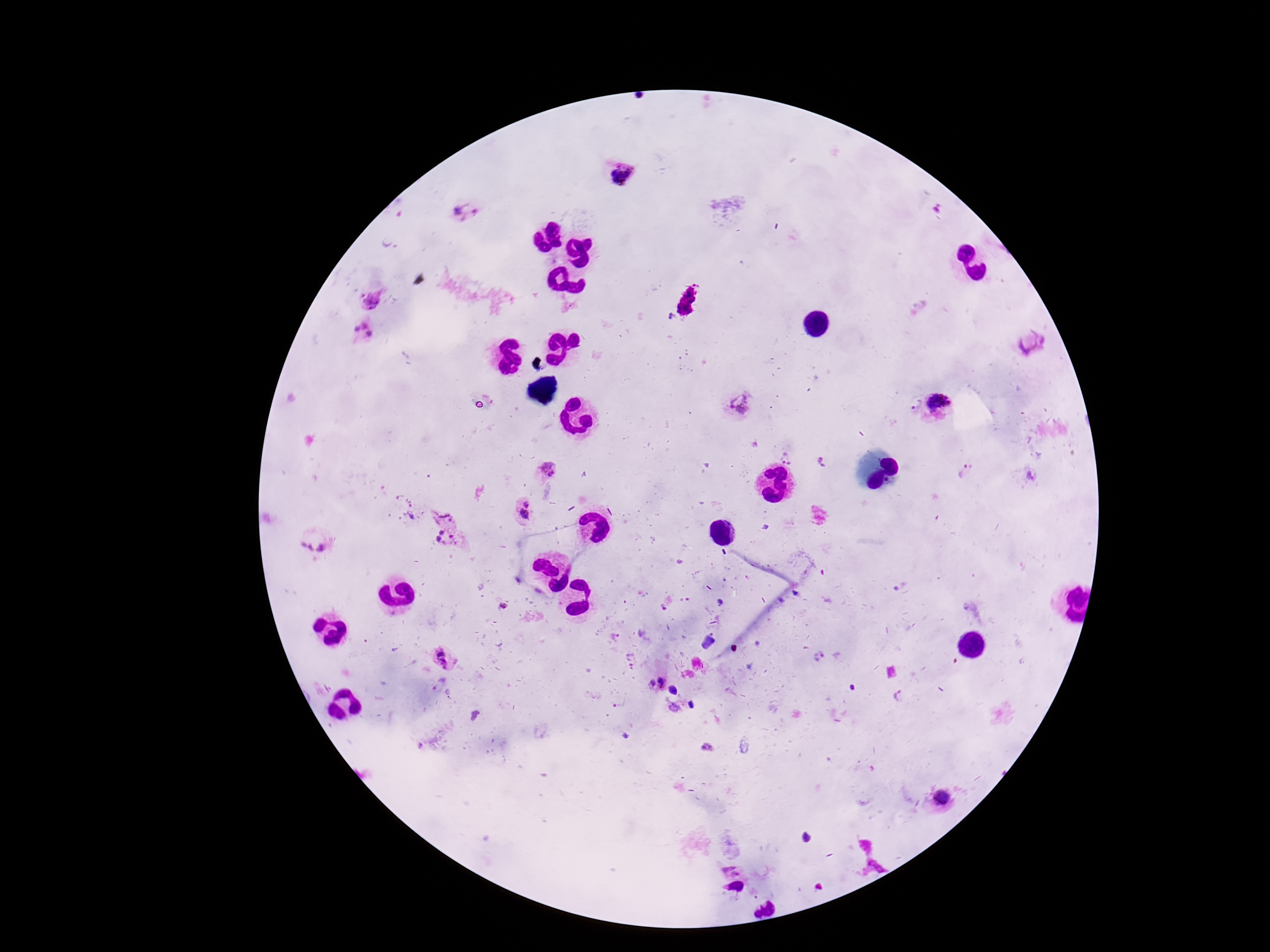
capture = smartphone camera through the microscope eyepiece
preparation = thick blood film
field of view = single
Plasmodium parasite locations = approximate centers as {x, y} in pixels: {621, 177}, {462, 212}, {373, 303}, {360, 334}, {1029, 344}, {913, 405}, {939, 407}, {738, 408}, {788, 452}, {548, 468}, {968, 471}, {409, 508}, {523, 512}, {444, 513}, {315, 545}, {447, 545}, {446, 659}, {656, 682}, {672, 689}, {942, 799}, {729, 868}, {736, 888}
image size = 1270×952 pixels
patient malaria status = infected
magnification = 100x
stain = Giemsa